Assess this cell for malaria.
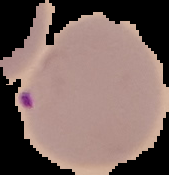

Parasitized.

Image is 169×175 pixels. Cell region segmented out of the field of view; the surrounding area is masked to black. From a thin blood film.